State which cell type is depicted.
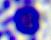
A leukocyte.

Summary:
  - Modality: photomicrograph
  - Magnification: 400x